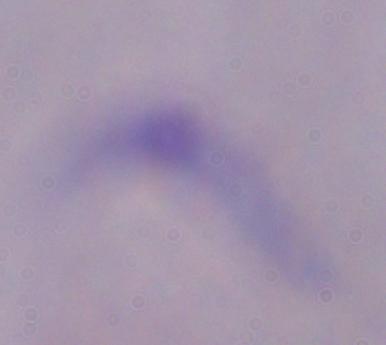
Summary:
  - Identification: trypanosome
  - Modality: micrograph
  - Magnification: 1000x